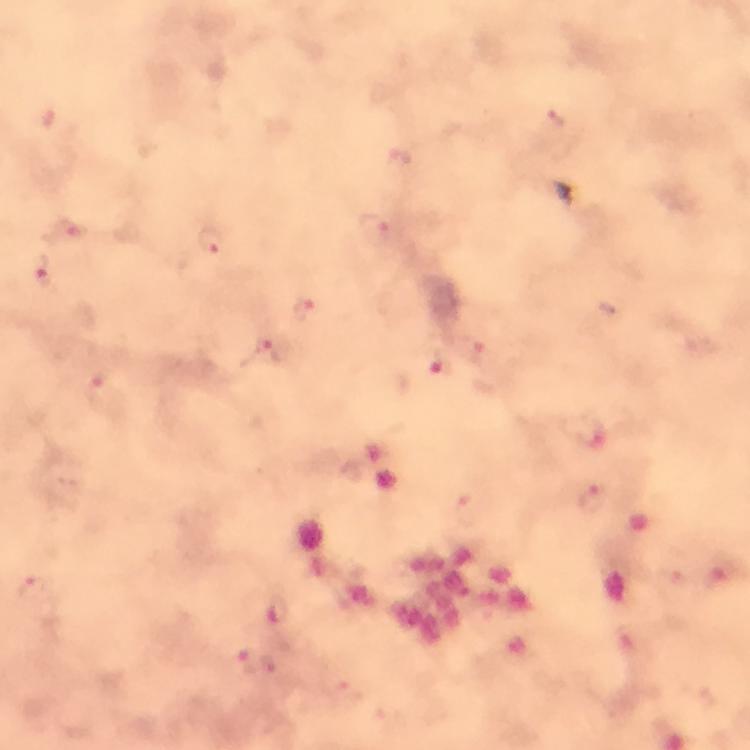

Approximate centers as {x, y} in pixels. Malaria parasite locations: {376, 226}, {68, 227}, {212, 242}, {43, 271}, {302, 309}, {265, 349}, {476, 352}, {440, 366}, {101, 391}, {584, 430}, {594, 501}, {279, 613}, {246, 661}, {269, 667}. Cropped region of a single field of view. Immersion oil was used. Thick smear. From a malaria diagnostic workup. At 100x magnification. Smartphone photograph taken through a microscope. Giemsa stain. Image is 750×750 pixels.